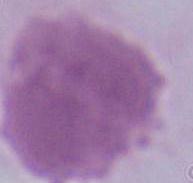

A red blood cell is shown. Captured at 1000x magnification. Photomicrograph.